State which parasite is depicted.
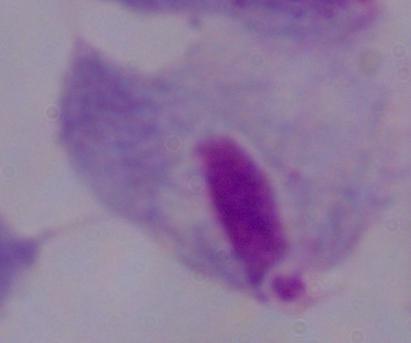
This is a trichomonad.

{
  "modality": "micrograph",
  "magnification": "1000x"
}